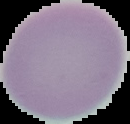

result = no Plasmodium parasites detected
image type = segmented cell region with the area outside set to black
image size = 130×124 pixels
preparation = thin blood film